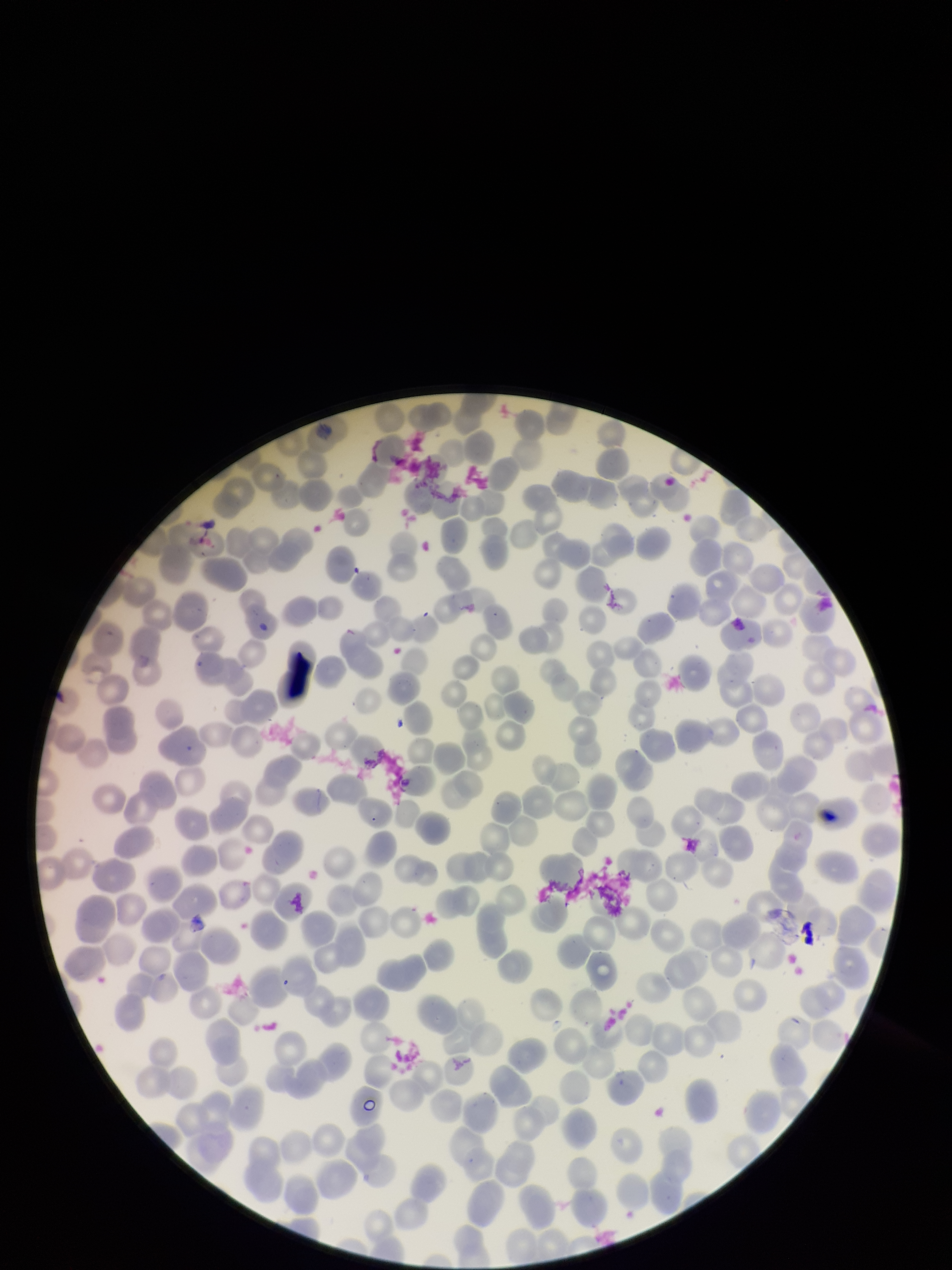

Photographed through the microscope eyepiece with a smartphone camera. Red blood cell count: 272. Image is 952×1270 pixels. One field from this slide. Preparation: thin. Parasitized red blood cells: none seen. Patient malaria status: negative. Parasitized red blood cell count: 0. Stained with Giemsa.